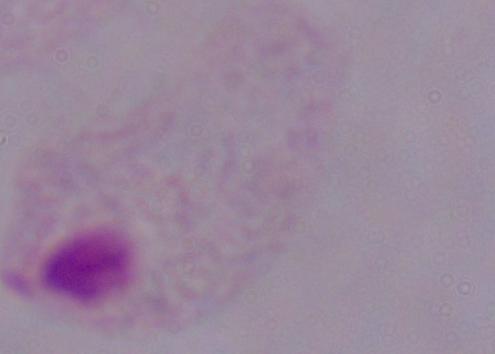

magnification: 1000x
modality: micrograph
identification: trichomonad